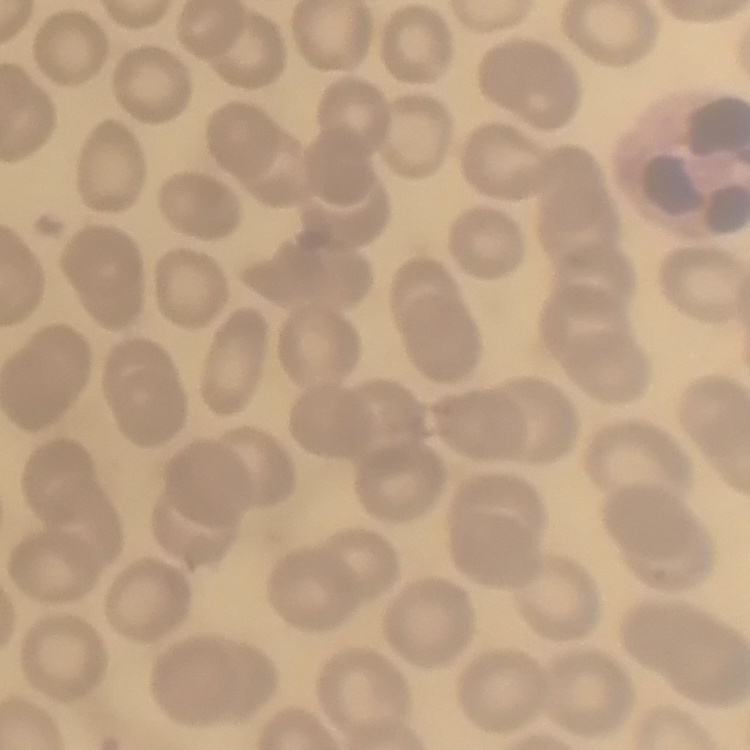

{
  "red_blood_cell_morphology": "no rouleaux formation",
  "preparation": "thin peripheral smear",
  "image_type": "one tile cut from a larger photomicrograph",
  "stain": "Field's or Giemsa"
}